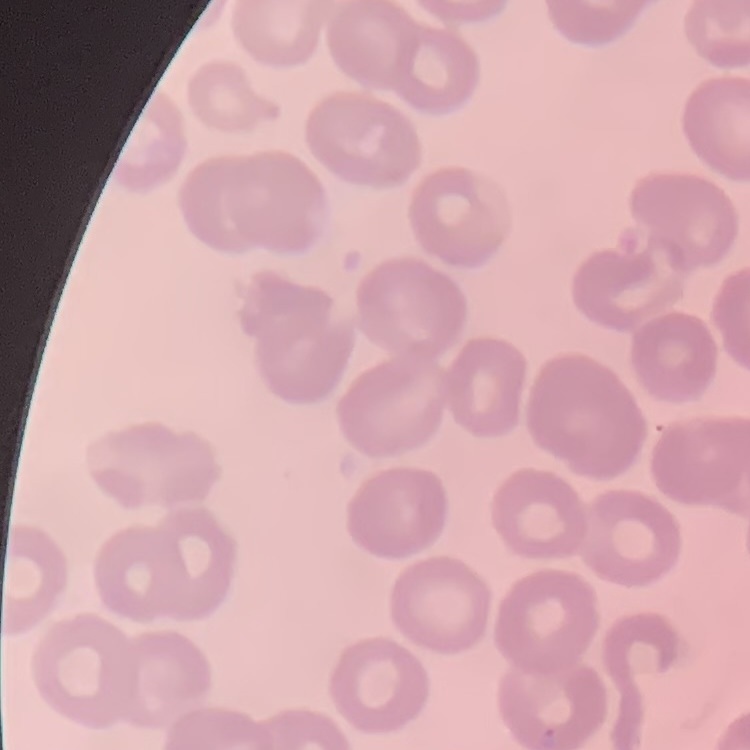

Summary:
  - Red blood cell morphology: no rouleaux formation
  - Stain: Field's or Giemsa
  - Preparation: thin blood film
  - Image type: square crop of a larger photomicrograph